Assess this cell for malaria.
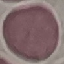
It is uninfected.

preparation = thin smear
capture = smartphone camera at the microscope eyepiece
stain = Giemsa
image type = automatically extracted cell patch, resized to 64 × 64 pixels